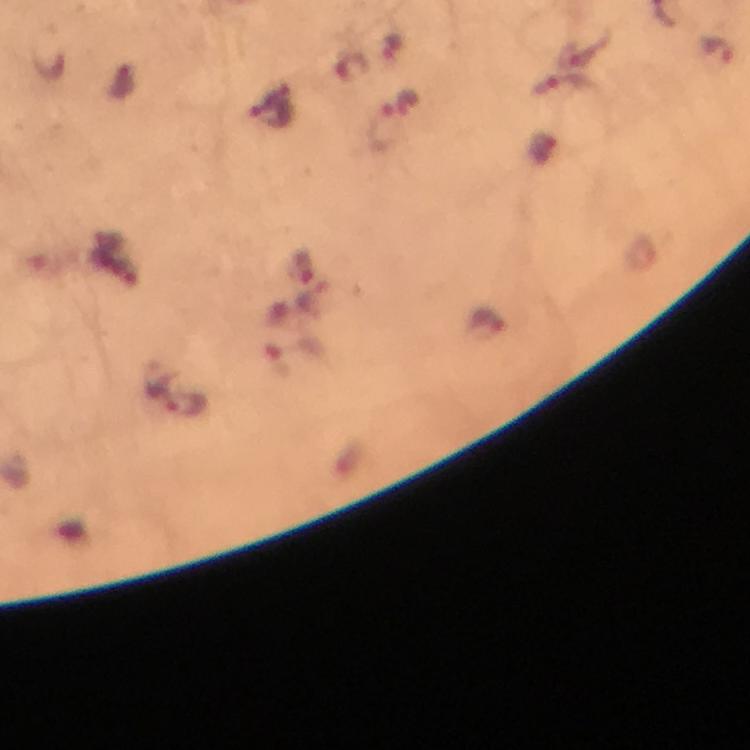
Approximate centers as {x, y} in pixels.
Summary:
  - Plasmodium parasite locations: {719, 51}, {562, 84}, {272, 113}, {380, 127}, {188, 403}
  - Image size: 750×750 pixels
  - Preparation: thick smear
  - Context: from a diagnostic examination for malaria
  - Capture: smartphone camera through the microscope
  - Magnification: 100x
  - Cropped from: one field of view
  - Immersion oil: used
  - Stain: Giemsa